State the blood parasite species.
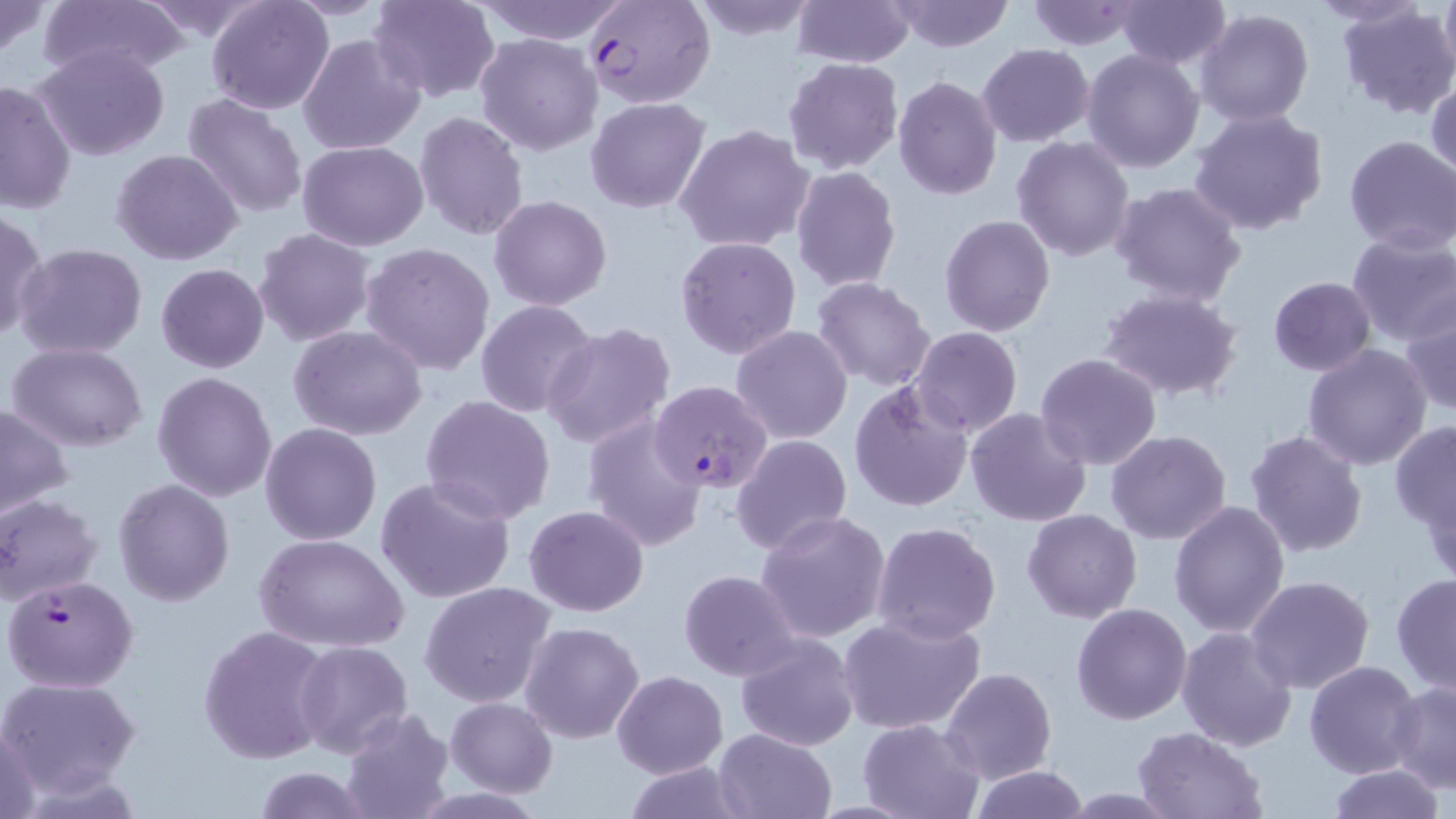
Plasmodium falciparum.

Summary:
  - Coordinate format: approximate bounding boxes as (x1,y1)-(x2,y2) corner pairs in pixels
  - Plasmodium falciparum-infected red blood cell locations: (584,0)-(715,110), (650,381)-(772,493), (3,573)-(138,693)
  - Uninfected red blood cell locations: (0,0)-(52,58), (38,0)-(188,82), (136,0)-(272,44), (206,0)-(333,115), (285,0)-(392,19), (369,0)-(500,103), (476,0)-(626,45), (684,0)-(820,41), (792,0)-(914,67), (892,0)-(1015,53), (1116,0)-(1229,69), (1308,0)-(1427,26), (1439,0)-(1456,78), (1024,1)-(1140,50), (1337,4)-(1456,117), (1195,8)-(1315,128), (1090,26)-(1300,150), (475,33)-(603,155), (297,34)-(423,156), (32,43)-(173,163), (976,43)-(1095,147), (1081,47)-(1204,172), (783,57)-(905,173), (892,75)-(1004,199), (0,77)-(77,215), (1427,77)-(1456,187), (182,93)-(308,219), (586,98)-(710,214), (1189,107)-(1329,236), (413,111)-(528,243), (673,124)-(816,253), (1344,134)-(1456,254), (1012,135)-(1136,261), (298,140)-(430,251), (112,148)-(243,265), (789,166)-(902,294), (1110,181)-(1248,308), (489,195)-(612,311), (0,206)-(46,341), (939,214)-(1055,337), (253,228)-(376,348), (1346,230)-(1456,347), (675,234)-(802,359), (360,242)-(495,376), (12,243)-(150,362), (155,263)-(270,373), (811,276)-(937,390), (1268,277)-(1377,374), (1099,288)-(1244,402), (476,300)-(599,419), (1403,301)-(1455,415), (542,323)-(675,449), (730,326)-(854,446), (288,327)-(428,441), (907,327)-(1023,438), (7,341)-(150,452), (1302,342)-(1432,469), (1034,353)-(1163,473), (151,371)-(276,502), (848,382)-(973,513), (421,394)-(555,524), (0,404)-(74,520), (965,408)-(1093,529), (581,414)-(708,553), (1390,421)-(1456,531), (260,423)-(382,546), (1244,428)-(1367,559), (1107,429)-(1232,544), (732,434)-(852,555), (1421,475)-(1456,590), (374,477)-(517,607), (113,479)-(235,605), (0,494)-(103,607), (1169,500)-(1291,637), (524,504)-(650,616), (1023,509)-(1142,622), (756,510)-(892,645), (872,521)-(1001,642), (256,533)-(410,654), (679,569)-(801,680), (1391,572)-(1456,696), (1245,575)-(1374,694), (419,581)-(558,708), (1070,602)-(1193,726), (837,612)-(988,737), (519,621)-(645,744), (197,624)-(332,764), (1175,624)-(1297,752), (734,632)-(859,753), (295,640)-(413,758), (1304,659)-(1425,779), (939,666)-(1056,784), (611,670)-(727,777), (0,675)-(142,797), (1389,679)-(1456,792), (445,697)-(557,796), (338,707)-(455,819), (856,718)-(985,819), (0,721)-(45,819), (712,728)-(838,819), (1133,729)-(1266,817), (620,761)-(754,818), (1325,764)-(1445,819), (967,765)-(1091,819), (250,766)-(372,819)
  - Image size: 1456×819 pixels
  - Field of view: one of a larger specimen
  - Stain: May-Grünwald-Giemsa
  - Preparation: thin blood smear
  - Magnification: 1000x
  - Modality: optical microscopy